Identify the cell.
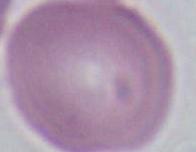
An erythrocyte.

Micrograph. Captured at 1000x magnification.